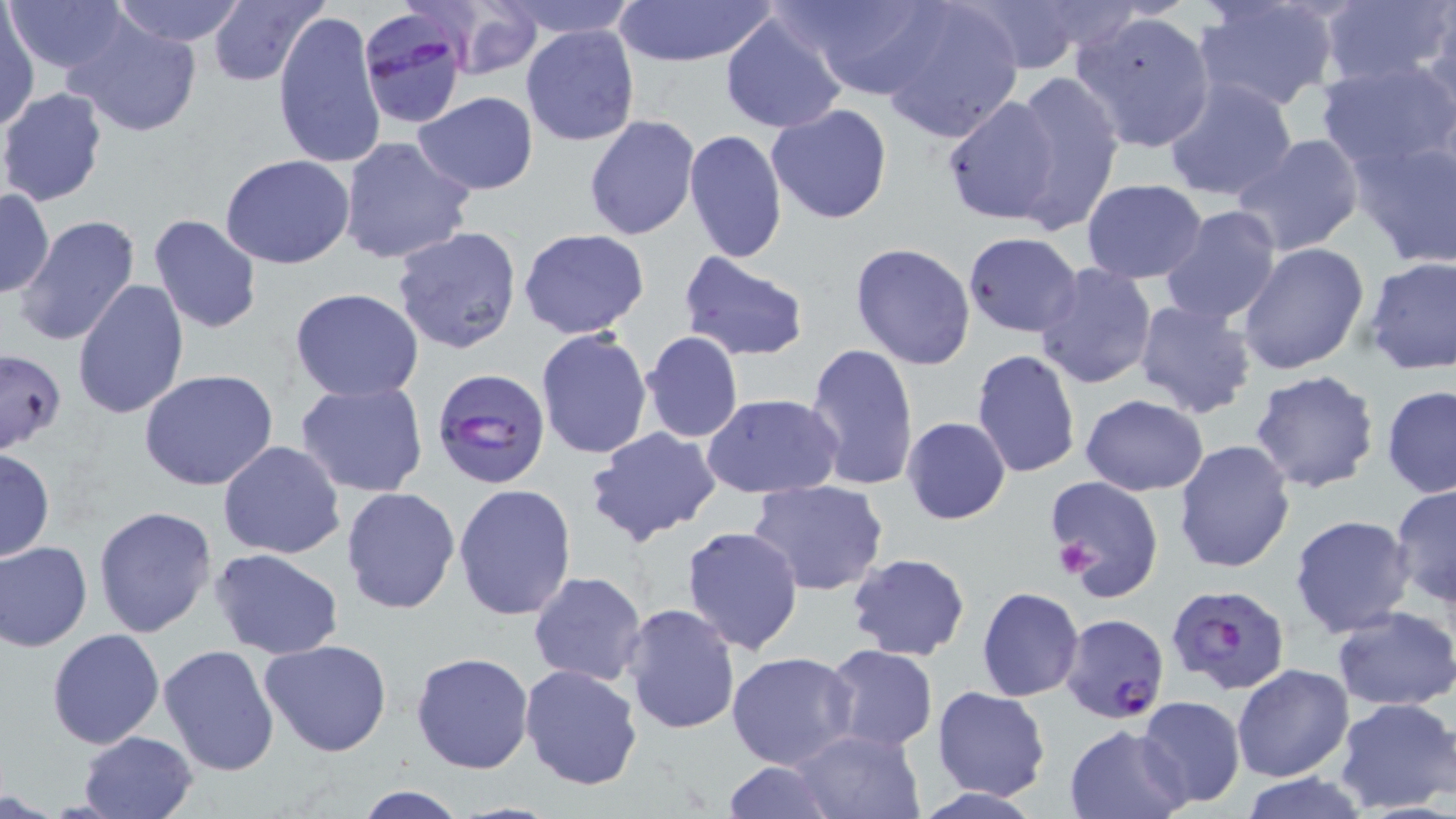
Approximate bounding boxes as (x1, y1, x2, y2) in pixels. Uninfected red blood cell locations: (4, 0, 129, 77), (110, 0, 249, 47), (207, 0, 325, 88), (493, 0, 643, 39), (609, 0, 778, 65), (782, 0, 951, 99), (877, 0, 1026, 142), (960, 0, 1094, 74), (1193, 0, 1339, 112), (1320, 0, 1456, 91), (436, 2, 544, 82), (272, 7, 386, 173), (1423, 7, 1456, 124), (720, 9, 849, 134), (1071, 10, 1217, 152), (1, 11, 39, 131), (64, 13, 204, 139), (520, 24, 640, 147), (1316, 60, 1456, 172), (1010, 70, 1125, 234), (1161, 77, 1299, 203), (0, 88, 108, 207), (413, 91, 539, 195), (941, 94, 1064, 225), (766, 104, 894, 225), (584, 116, 701, 241), (684, 129, 788, 262), (1349, 133, 1456, 270), (1232, 134, 1365, 257), (337, 136, 475, 266), (221, 154, 356, 269), (1081, 179, 1208, 283), (1, 188, 55, 296), (1159, 204, 1283, 327), (12, 213, 142, 347), (148, 213, 262, 335), (392, 224, 525, 356), (518, 228, 649, 339), (962, 232, 1083, 337), (849, 241, 977, 370), (1237, 242, 1371, 377), (678, 249, 811, 360), (1362, 255, 1454, 376), (1033, 262, 1160, 392), (72, 278, 191, 420), (289, 288, 426, 402), (1132, 299, 1259, 421), (639, 330, 745, 444), (533, 331, 653, 461), (804, 343, 918, 490), (3, 348, 67, 451), (971, 349, 1082, 479), (138, 370, 280, 492), (1249, 370, 1381, 494), (294, 381, 429, 498), (1381, 384, 1456, 498), (701, 392, 844, 499), (1079, 394, 1209, 496), (901, 415, 1012, 524), (586, 426, 723, 547), (1173, 438, 1296, 575), (217, 440, 347, 559), (0, 447, 54, 563), (1045, 475, 1163, 600), (746, 479, 889, 597), (453, 482, 578, 619), (1390, 483, 1456, 609), (340, 485, 462, 616), (93, 505, 217, 638), (1289, 513, 1416, 638), (681, 526, 804, 655), (1, 540, 93, 651), (211, 549, 346, 659), (846, 551, 972, 661), (528, 571, 648, 687), (977, 587, 1084, 701), (621, 604, 741, 735), (1332, 605, 1456, 711), (47, 628, 165, 749), (259, 639, 393, 757), (157, 643, 281, 777), (824, 644, 939, 751), (727, 649, 858, 771), (410, 651, 535, 775), (518, 664, 644, 791), (1233, 664, 1354, 781), (931, 686, 1053, 801), (1135, 696, 1247, 807), (1333, 697, 1456, 814), (1064, 723, 1190, 818), (789, 727, 924, 818), (77, 730, 198, 819), (718, 760, 838, 819), (1235, 771, 1375, 818), (353, 786, 469, 819). Platelet locations: (1054, 539, 1099, 578). Plasmodium falciparum-infected red blood cell locations: (357, 10, 472, 133), (431, 367, 551, 492), (1165, 583, 1292, 696), (1060, 612, 1170, 722). Slide-level diagnosis: Plasmodium falciparum. Captured at 1000x magnification. Image is 1456×819 pixels. Single field of view. Thin blood film. May-Grünwald-Giemsa-stained preparation. Light microscopy.